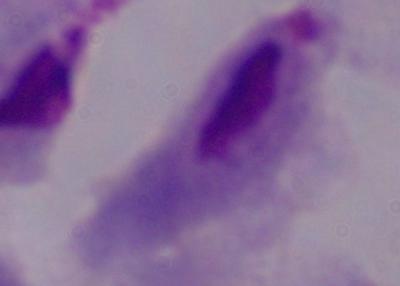
Summary:
  - Identification: trichomonad
  - Magnification: 1000x
  - Modality: photomicrograph